Locate every Plasmodium parasite.
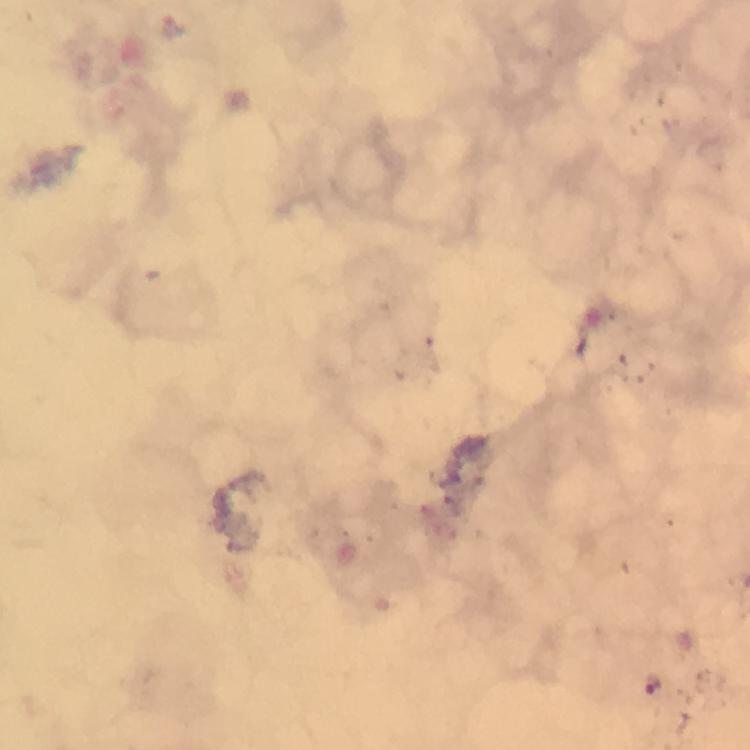
Approximate centers as (x, y) in pixels.
Plasmodium parasites: (653, 683).

Photographed through the microscope with a smartphone camera. Immersion oil was used. At 100x magnification. Thick smear. From a malaria diagnostic workup. Image is 750×750 pixels. A crop from one field of view. Giemsa-stained preparation.